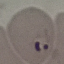 Malaria status: parasitized. Giemsa stain. Automatically extracted cell patch, resized to 64 × 64 pixels. Acquired by smartphone through the microscope eyepiece. Thin smear of blood.